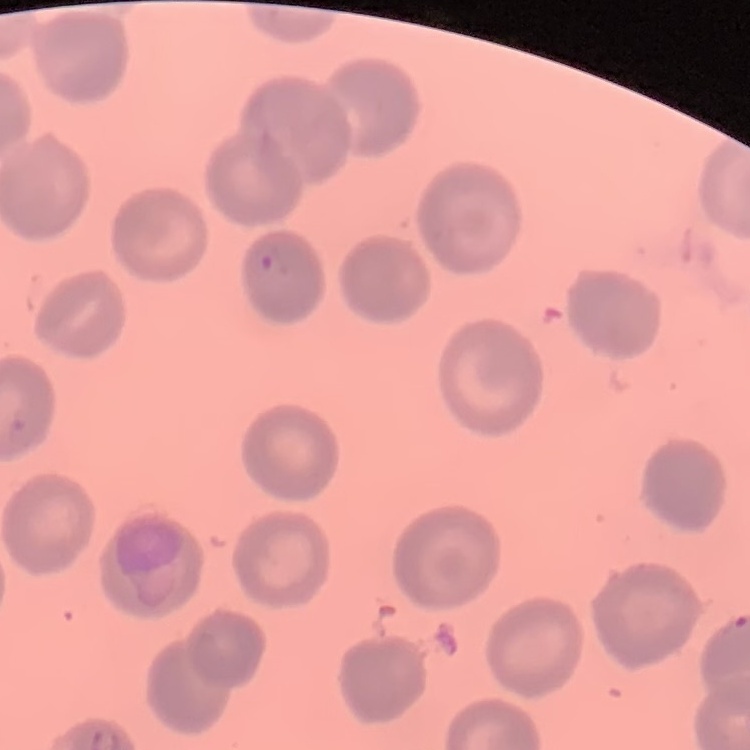
Summary:
  - Erythrocyte morphology: no rouleaux formation
  - Preparation: thin peripheral smear
  - Image type: one tile cut from a larger photomicrograph
  - Stain: Field's or Giemsa